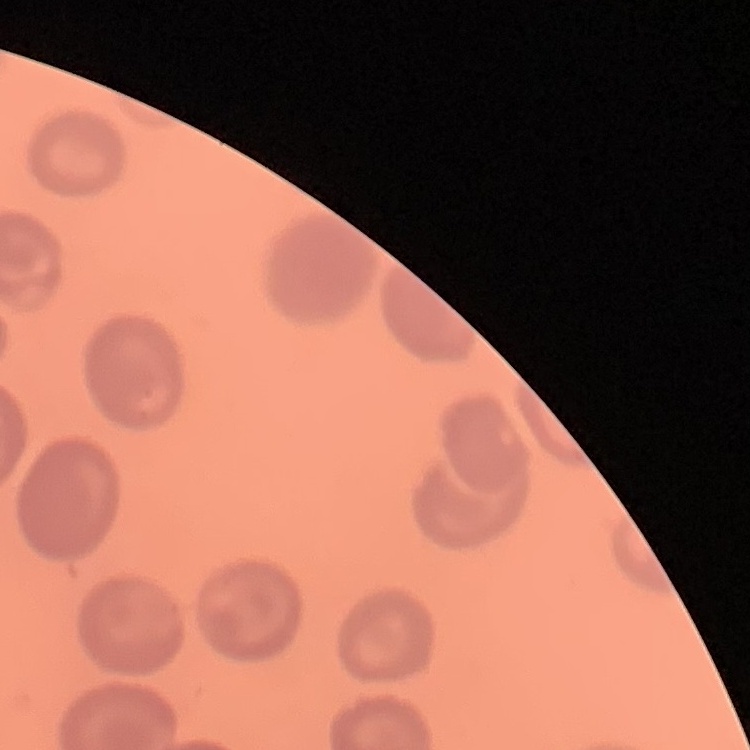
red blood cell morphology = no rouleaux formation
stain = Field's or Giemsa
preparation = thin blood film
image type = one tile cut from a larger photomicrograph